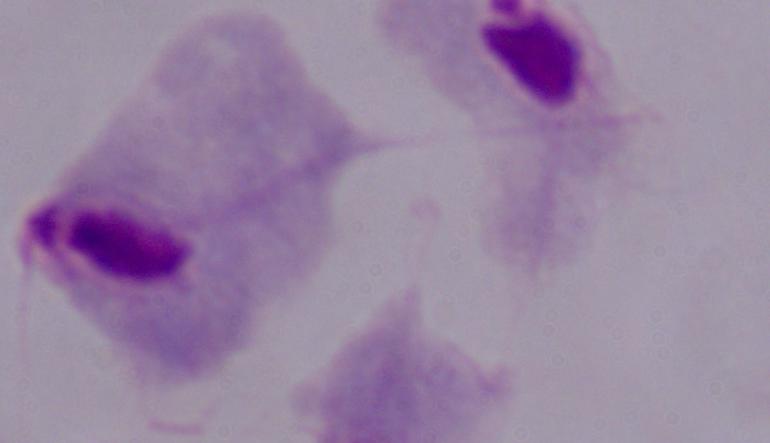 Photomicrograph. Captured at 1000x magnification. A trichomonad is seen.